Point out each Plasmodium parasite.
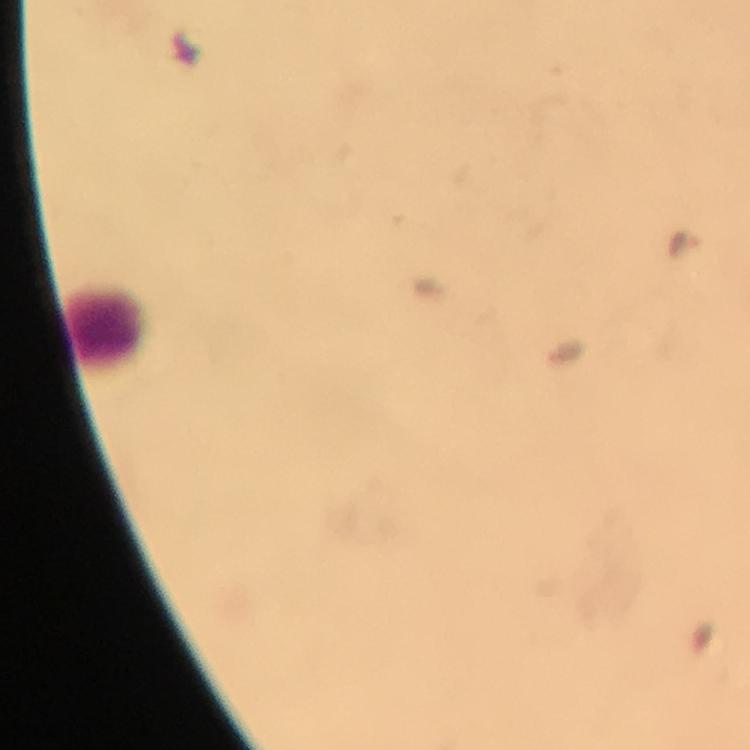
Approximate centers as (x, y) in pixels.
Plasmodium parasites: (685, 245).

Leukocyte locations: (105, 320). 100x magnification. Photographed with a smartphone mounted on the microscope. Thick blood smear. Image is 750×750 pixels. Giemsa-stained preparation. Immersion oil was used. A crop from one field of view. From a malaria diagnostic workup.